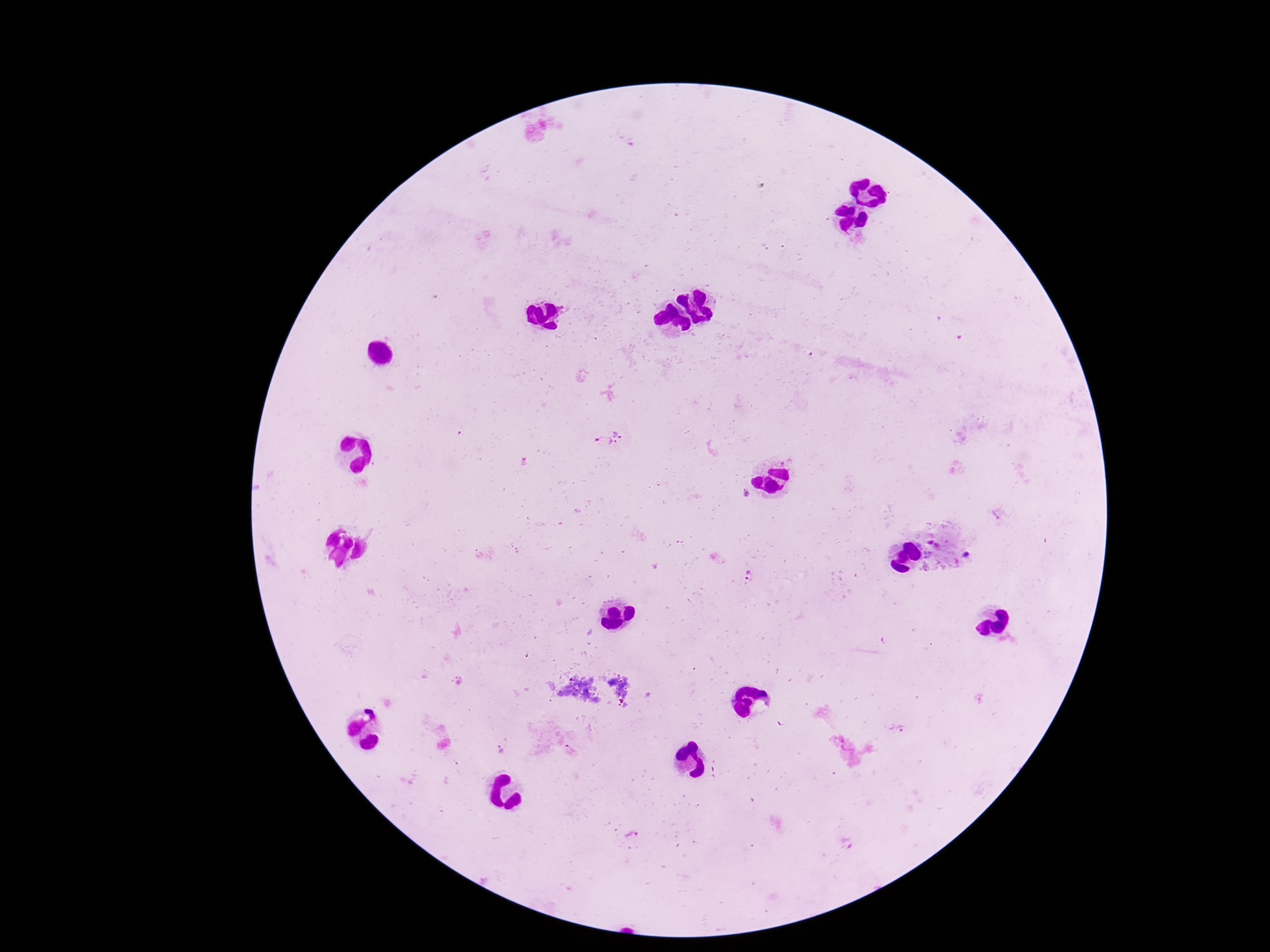

field of view = single
preparation = thick peripheral-blood smear
Plasmodium parasite locations = approximate centers as (x, y) in pixels: (609, 437), (749, 579), (500, 751), (571, 751), (633, 835)
capture = smartphone camera through the microscope eyepiece
magnification = 100x
stain = Giemsa
image size = 1270×952 pixels
patient malaria status = positive